Locate every blood parasite and identify its species.
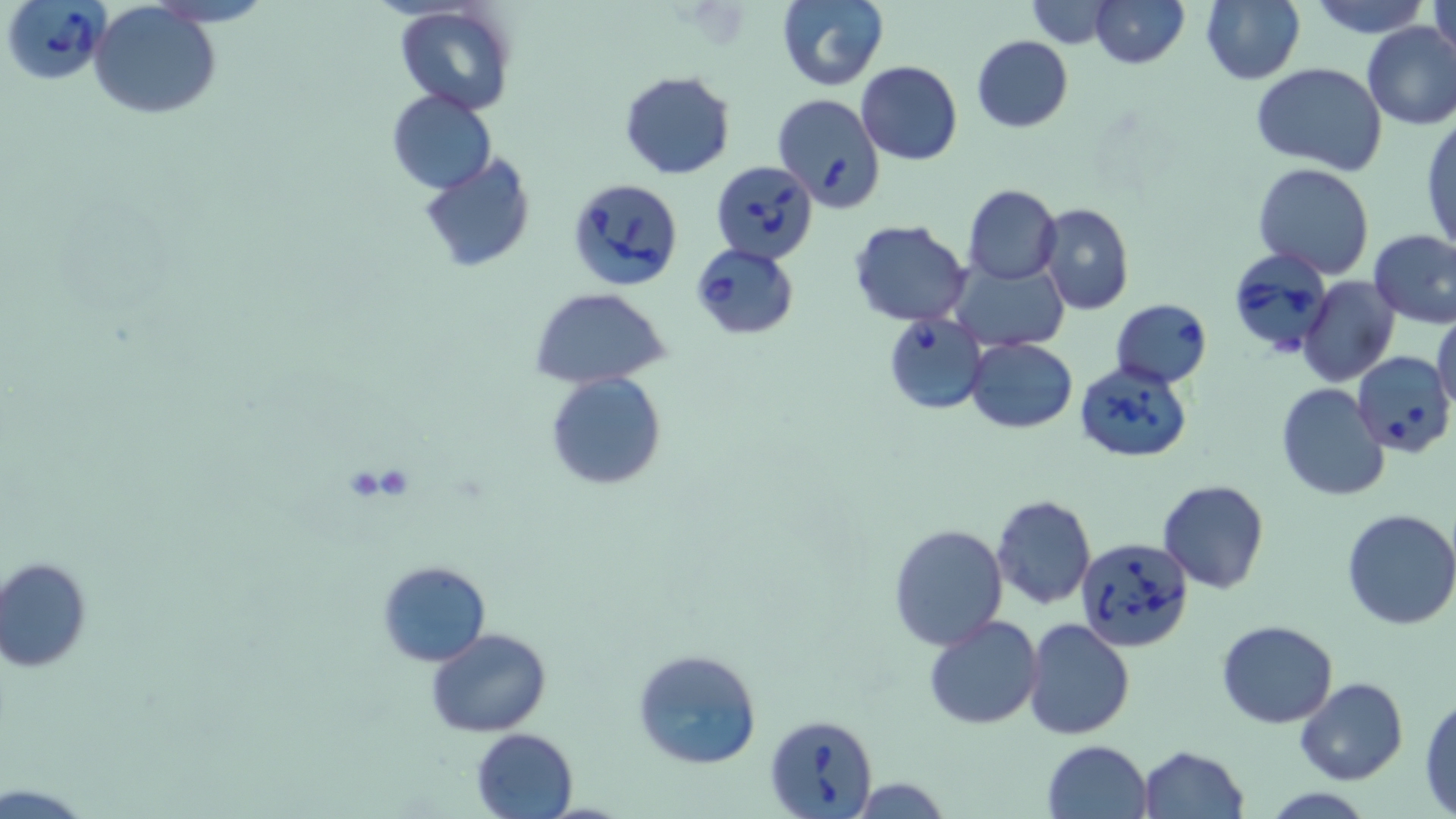
Approximate bounding boxes as (x1, y1, x2, y2) in pixels.
Babesia divergens-infected red blood cells: (2, 2, 112, 89), (771, 93, 886, 211), (711, 160, 817, 264), (565, 178, 684, 291), (690, 242, 798, 340), (1225, 249, 1334, 359), (1110, 299, 1212, 388), (882, 311, 988, 414), (1353, 351, 1455, 459), (1073, 363, 1191, 465), (1075, 537, 1194, 652), (765, 712, 879, 819).
No Plasmodium falciparum, Plasmodium ovale, Plasmodium malariae, Plasmodium vivax, or Trypanosoma brucei observed.

Summary:
  - Uninfected red blood cell locations: (775, 0, 889, 92), (1089, 0, 1190, 69), (1199, 0, 1305, 86), (1313, 0, 1427, 38), (1429, 0, 1455, 65), (1023, 1, 1119, 48), (395, 2, 517, 117), (89, 4, 222, 118), (1361, 21, 1456, 130), (971, 36, 1072, 133), (856, 61, 963, 165), (1251, 63, 1389, 173), (619, 70, 735, 180), (387, 92, 496, 193), (1421, 114, 1455, 256), (419, 153, 538, 273), (1253, 163, 1376, 280), (962, 184, 1062, 285), (1035, 203, 1134, 316), (848, 220, 973, 326), (1369, 229, 1456, 328), (949, 257, 1069, 353), (1299, 276, 1400, 386), (530, 287, 670, 388), (1431, 310, 1456, 416), (966, 337, 1077, 434), (545, 372, 667, 492), (1274, 384, 1390, 502), (1157, 479, 1270, 594), (991, 494, 1096, 609), (1340, 508, 1456, 631), (887, 521, 1009, 651), (1, 557, 92, 672), (375, 560, 491, 667), (922, 615, 1043, 730), (1023, 619, 1135, 739), (1216, 619, 1338, 729), (427, 627, 552, 738), (631, 647, 763, 773), (1295, 676, 1408, 786), (1419, 693, 1456, 814), (471, 728, 578, 817), (1042, 740, 1154, 819), (1138, 745, 1250, 819), (847, 776, 955, 817)
  - Slide-level diagnosis: Babesia divergens
  - Magnification: 1000x
  - Field of view: one of a larger specimen
  - Modality: optical microscopy
  - Stain: May-Grünwald-Giemsa
  - Preparation: thin blood film
  - Image size: 1456×819 pixels